Evaluate for malaria.
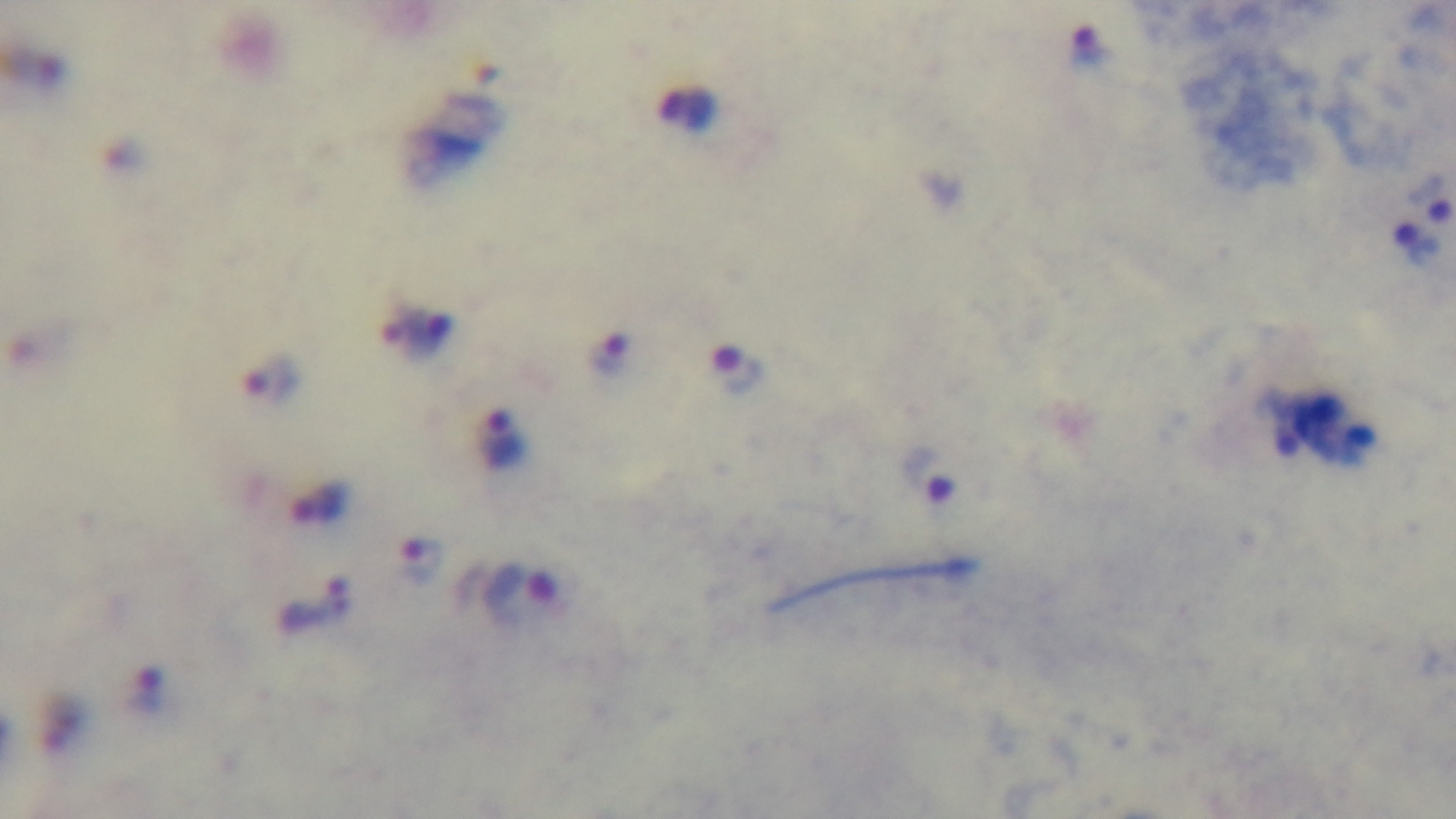
Positive.

stain = Giemsa
field of view = one from the slide
capture = mounted 4K digital camera
modality = light microscopy
preparation = thick smear
objective = 100x oil immersion